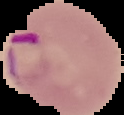

From a thin blood film. Cell region segmented out of the field of view; the surrounding area is masked to black. Image is 124×115 pixels. Malaria status: parasitized.